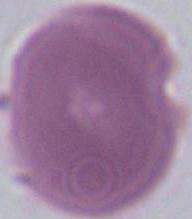 Micrograph. A red blood cell is seen. 1000x magnification.